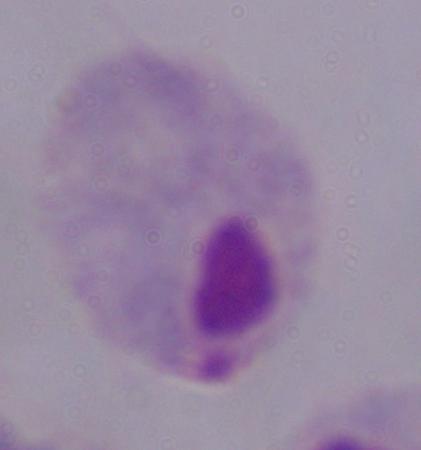
Summary:
  - Identification: trichomonad
  - Modality: micrograph
  - Magnification: 1000x